State which cell type is depicted.
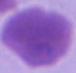

This is an erythrocyte.

Captured at 1000x magnification. Photomicrograph.